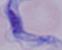

Captured at 1000x magnification. A trypanosome is shown. Micrograph.